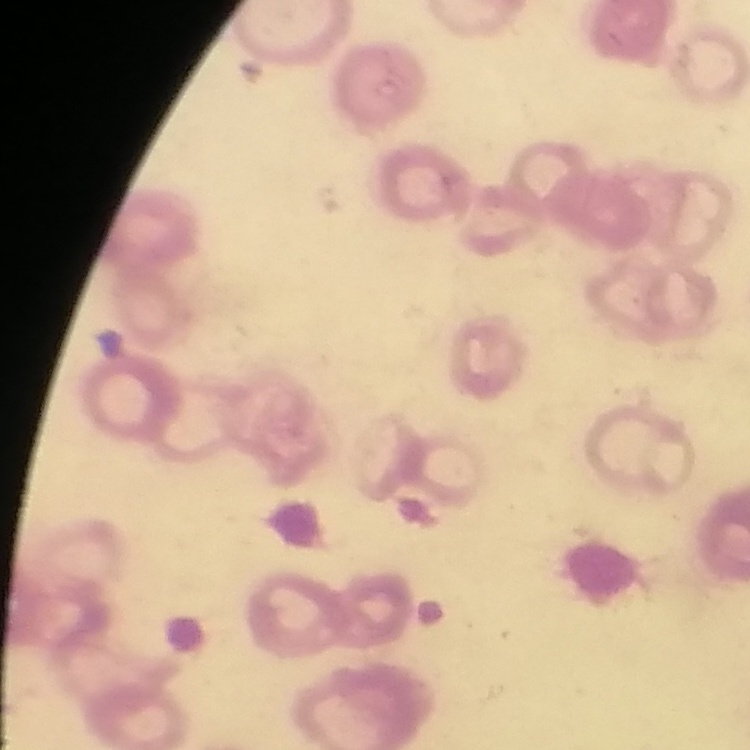 The red blood cells exhibit rouleaux formation. Thin blood smear. Square crop of a larger photomicrograph. Stained with either Field's or Giemsa.